Assess this cell for malaria.
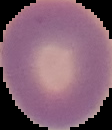
It is uninfected.

Cell region segmented out of the field of view; the surrounding area is masked to black. Image is 112×130 pixels. From a thin blood film.